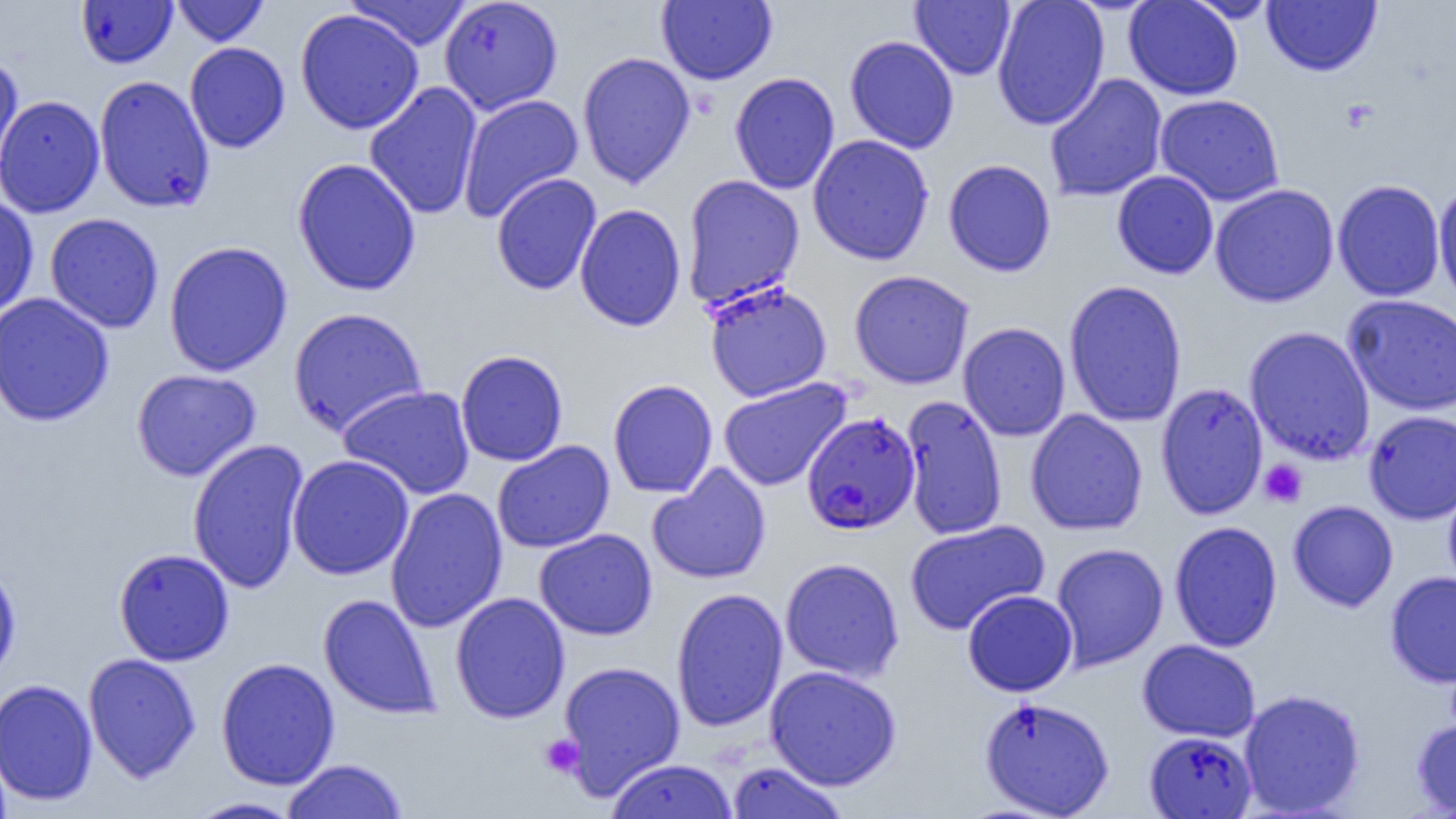

Summary:
  - Coordinate format: approximate bounding boxes as [x1, y1, x2, y2] in pixels
  - Platelet locations: [1259, 459, 1307, 507], [540, 733, 584, 778]
  - Uninfected red blood cell locations: [75, 0, 178, 69], [171, 0, 270, 45], [344, 0, 473, 51], [439, 0, 563, 115], [657, 0, 777, 85], [991, 0, 1110, 130], [1124, 0, 1243, 100], [1182, 0, 1281, 23], [910, 1, 1015, 80], [1262, 1, 1382, 76], [295, 9, 424, 134], [844, 35, 959, 154], [184, 42, 290, 153], [577, 52, 696, 188], [0, 54, 25, 185], [730, 72, 840, 194], [1044, 73, 1168, 202], [94, 75, 215, 213], [364, 82, 483, 220], [1155, 93, 1285, 206], [0, 94, 105, 219], [458, 94, 584, 222], [808, 134, 934, 265], [293, 158, 421, 296], [943, 158, 1056, 277], [1112, 170, 1219, 279], [491, 172, 602, 296], [682, 174, 804, 308], [1332, 179, 1446, 302], [1210, 183, 1339, 308], [1433, 183, 1456, 311], [0, 194, 39, 321], [574, 203, 686, 332], [45, 213, 164, 333], [163, 241, 294, 376], [849, 269, 975, 389], [1064, 279, 1186, 427], [704, 281, 832, 402], [0, 292, 114, 427], [1343, 294, 1456, 416], [287, 306, 429, 437], [958, 322, 1071, 441], [1244, 326, 1376, 465], [455, 350, 568, 466], [131, 368, 261, 481], [719, 378, 851, 491], [608, 379, 718, 498], [1156, 382, 1269, 519], [338, 385, 475, 500], [901, 394, 1007, 541], [1025, 409, 1147, 536], [1363, 410, 1456, 524], [187, 438, 309, 594], [492, 440, 615, 553], [286, 454, 414, 580], [647, 463, 771, 585], [1443, 478, 1456, 598], [385, 487, 507, 633], [1288, 500, 1398, 612], [905, 520, 1050, 635], [1169, 521, 1283, 652], [534, 528, 657, 640], [1050, 542, 1168, 671], [113, 549, 235, 666], [780, 557, 904, 683], [0, 563, 22, 687], [1385, 571, 1456, 688], [670, 588, 788, 732], [962, 589, 1077, 697], [450, 592, 570, 723], [318, 594, 440, 719], [1137, 639, 1260, 742], [83, 652, 201, 783], [215, 657, 340, 790], [557, 660, 686, 798], [765, 665, 902, 791], [0, 678, 98, 806], [1239, 688, 1366, 817], [979, 696, 1115, 817], [1412, 714, 1456, 817], [1143, 731, 1256, 818], [281, 759, 409, 819], [604, 759, 739, 819], [725, 761, 851, 818], [186, 797, 303, 818]
  - Plasmodium falciparum-infected red blood cell locations: [801, 412, 921, 535]
  - Slide-level diagnosis: Plasmodium falciparum
  - Modality: optical microscopy
  - Magnification: 1000x
  - Field of view: single
  - Preparation: thin blood film
  - Image size: 1456×819 pixels